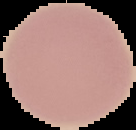

Summary:
  - Image size: 136×130 pixels
  - Preparation: thin blood film
  - Image type: segmented cell region with the area outside set to black
  - Malaria status: uninfected